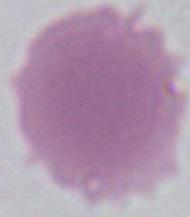
A red blood cell is seen. Captured at 1000x magnification. Micrograph.